Assess this cell for malaria.
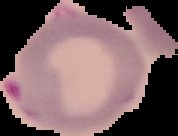
Parasitized.

Image is 178×136 pixels. From a thin blood smear. The area outside the segmented cell region is set to black.